Identify the parasite.
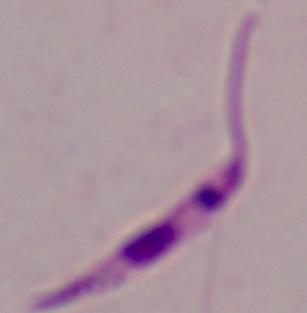
Leishmania.

Micrograph. 1000x magnification.